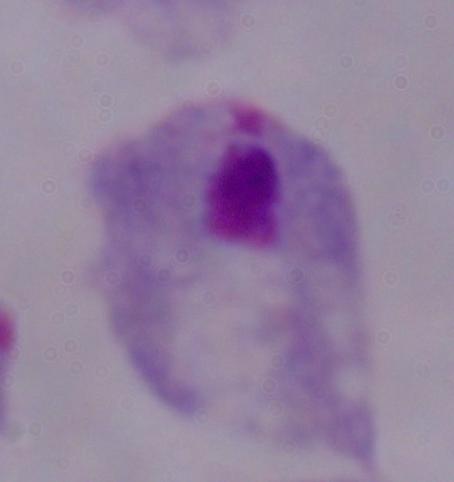

Captured at 1000x magnification. Micrograph. A trichomonad is shown.